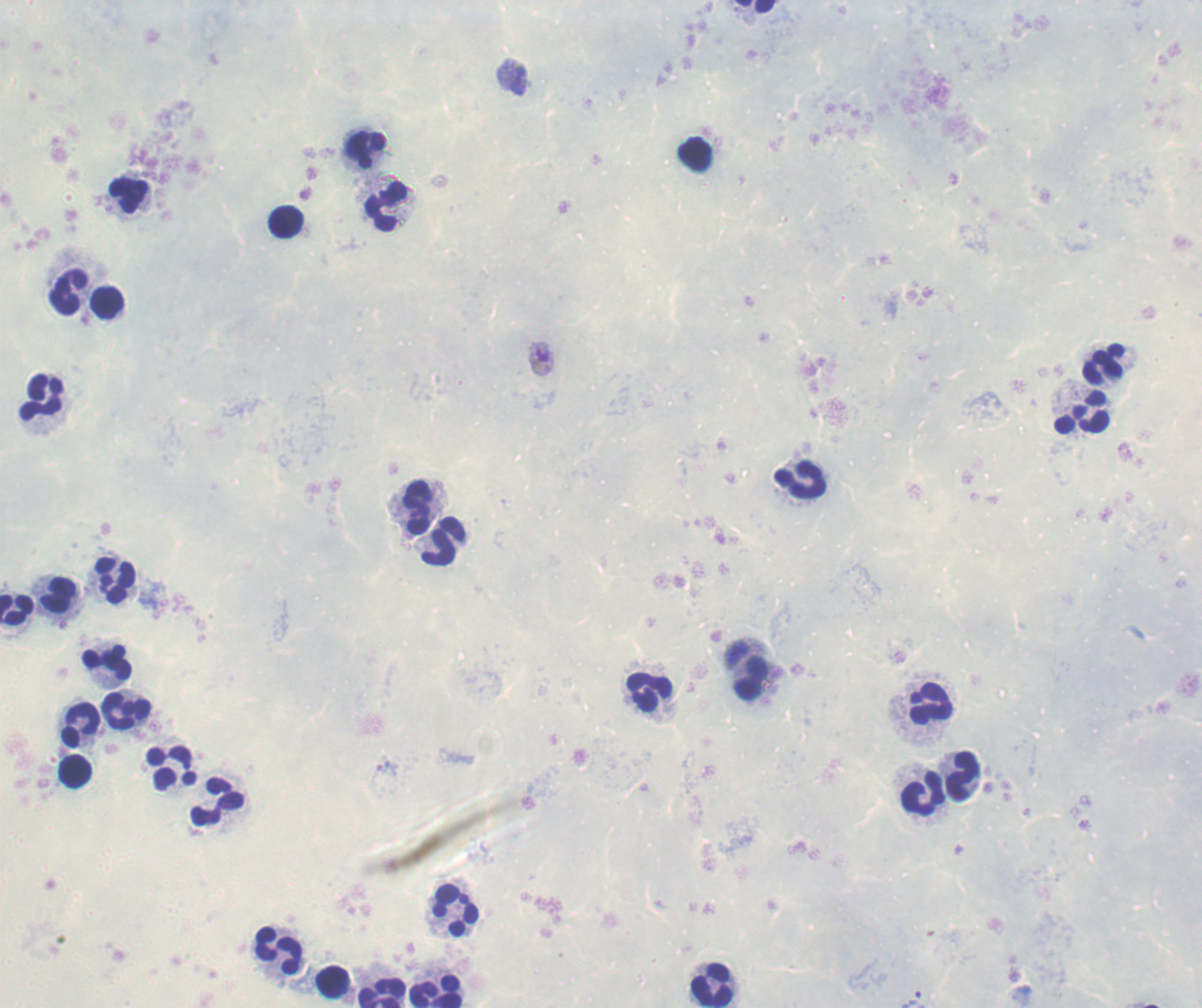
Approximate centers as [x, y] in pixels. Leukocyte locations: [756, 6], [366, 149], [697, 155], [130, 194], [384, 207], [287, 222], [68, 290], [108, 302], [1104, 364], [42, 397], [1082, 412], [801, 482], [415, 505], [445, 543], [116, 578], [60, 596], [16, 609], [106, 662], [748, 669], [651, 691], [928, 703], [127, 709], [80, 723], [174, 769], [74, 772], [964, 776], [922, 793], [218, 805], [454, 910], [280, 950], [333, 981], [713, 984], [436, 989], [381, 990]. Gametocyte locations: [540, 358]. Trophozoite locations: [513, 77], [910, 998]. Life-cycle stages observed: trophozoite, gametocyte. Background quality: unsatisfactory. Image is 1202×1008 pixels. Captured at 100x magnification. Thick blood smear. Romanowsky-stained preparation. Result: malaria parasites detected. Previously used in an actual diagnosis. One field from this slide.